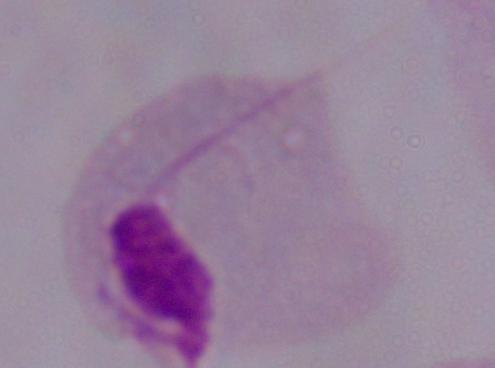

modality = photomicrograph
magnification = 1000x
identification = trichomonad